Comment on the morphology of the erythrocytes.
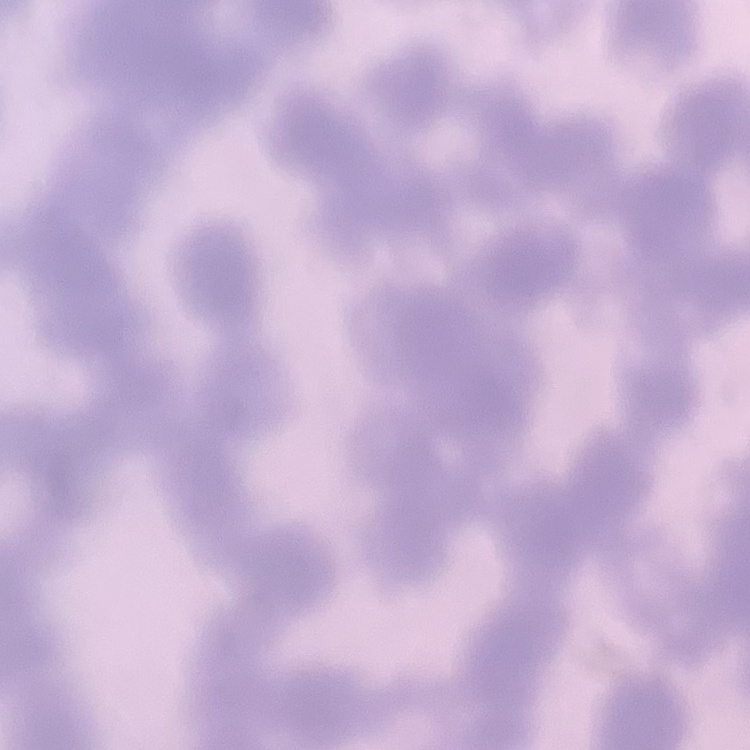
They show rouleaux formation.

{
  "image_type": "one tile cut from a larger photomicrograph",
  "stain": "Field's or Giemsa",
  "preparation": "thin blood film"
}